State which cell type is depicted.
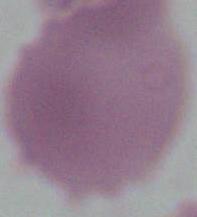
An erythrocyte.

Summary:
  - Magnification: 1000x
  - Modality: micrograph